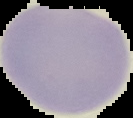
Result: negative for malaria parasites. The area outside the segmented cell region is set to black. Image is 133×118 pixels. From a thin blood smear.